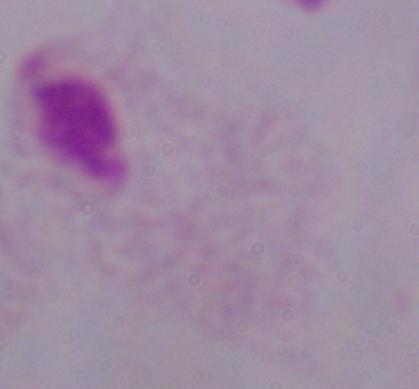
magnification: 1000x
identification: trichomonad
modality: micrograph